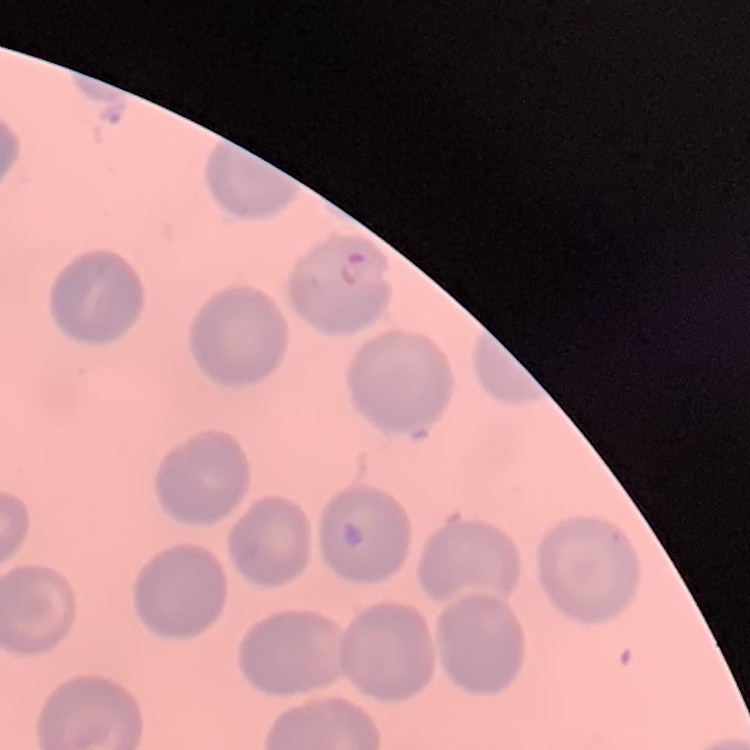
red blood cell morphology = no rouleaux formation
stain = Field's or Giemsa
preparation = thin peripheral smear
image type = square crop of a larger photomicrograph